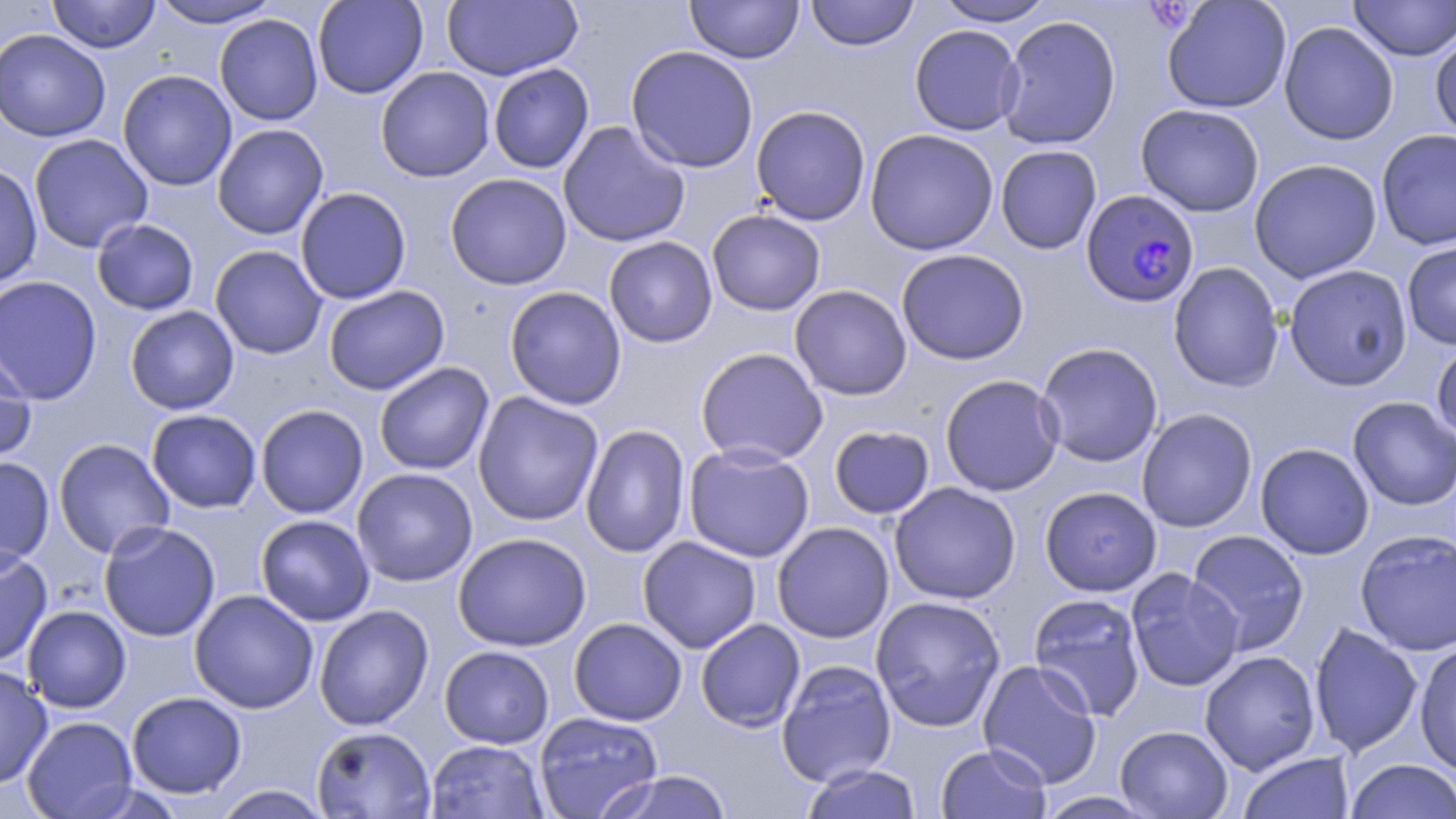

Summary:
  - Coordinate format: approximate bounding boxes as [x1, y1, x2, y2] in pixels
  - Plasmodium falciparum-infected red blood cell locations: [1080, 189, 1200, 308]
  - Uninfected red blood cell locations: [47, 0, 161, 53], [150, 0, 283, 29], [312, 0, 428, 99], [442, 0, 583, 81], [806, 0, 919, 51], [934, 0, 1058, 27], [1162, 0, 1291, 114], [1349, 0, 1455, 61], [685, 1, 803, 64], [214, 14, 323, 125], [997, 15, 1122, 150], [1273, 18, 1392, 278], [1279, 22, 1399, 145], [909, 24, 1023, 136], [0, 29, 111, 142], [1430, 31, 1456, 141], [625, 46, 759, 173], [488, 63, 594, 174], [375, 66, 495, 182], [117, 69, 237, 191], [1136, 103, 1264, 217], [751, 105, 871, 226], [557, 121, 690, 248], [212, 123, 329, 240], [864, 128, 999, 255], [1376, 129, 1456, 250], [28, 133, 153, 253], [995, 145, 1102, 254], [1249, 158, 1382, 283], [0, 164, 42, 289], [445, 173, 572, 290], [295, 187, 412, 305], [707, 209, 826, 316], [92, 219, 199, 315], [603, 236, 718, 348], [1402, 240, 1456, 350], [210, 245, 327, 359], [896, 248, 1029, 365], [1168, 262, 1284, 392], [1284, 264, 1412, 391], [0, 275, 103, 406], [789, 284, 912, 400], [323, 286, 450, 395], [504, 286, 627, 410], [125, 306, 239, 415], [1431, 341, 1456, 445], [1035, 342, 1163, 467], [0, 345, 37, 467], [695, 347, 828, 466], [374, 361, 494, 476], [940, 374, 1064, 497], [472, 391, 604, 526], [1348, 396, 1456, 511], [255, 404, 368, 519], [1136, 408, 1257, 533], [146, 409, 262, 513], [580, 424, 691, 559], [828, 425, 935, 519], [53, 438, 175, 558], [1255, 442, 1374, 559], [683, 443, 815, 562], [0, 456, 54, 569], [351, 468, 478, 587], [889, 481, 1021, 605], [1040, 486, 1162, 596], [255, 514, 375, 626], [99, 520, 221, 642], [772, 522, 894, 643], [1187, 529, 1309, 653], [1355, 530, 1456, 655], [453, 532, 592, 651], [637, 536, 761, 653], [0, 547, 52, 668], [1125, 568, 1243, 692], [189, 589, 319, 714], [1027, 593, 1147, 721], [870, 595, 1006, 732], [314, 604, 434, 730], [23, 605, 131, 713], [568, 618, 687, 726], [695, 618, 805, 732], [1309, 623, 1422, 757], [1414, 641, 1456, 777], [439, 645, 554, 749], [1199, 650, 1320, 774], [776, 659, 896, 787], [978, 659, 1103, 789], [0, 663, 53, 789], [127, 691, 247, 798], [534, 711, 663, 819], [22, 716, 138, 819], [311, 725, 436, 818], [1115, 725, 1232, 818], [425, 740, 548, 819], [936, 743, 1051, 818], [1237, 751, 1355, 819], [1344, 759, 1456, 818], [799, 764, 923, 819], [602, 770, 734, 819], [212, 785, 332, 818], [1035, 791, 1158, 818]
  - Slide-level diagnosis: Plasmodium falciparum
  - Image size: 1456×819 pixels
  - Preparation: thin blood film
  - Modality: optical microscopy
  - Magnification: 1000x
  - Stain: May-Grünwald-Giemsa
  - Field of view: one of a larger specimen